Report the malaria status of this cell.
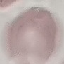
Uninfected.

Photographed with a smartphone camera at the microscope eyepiece. Thin blood smear. Cell patch, automatically extracted from a larger field of view and resized to 64 × 64 pixels. Giemsa-stained preparation.